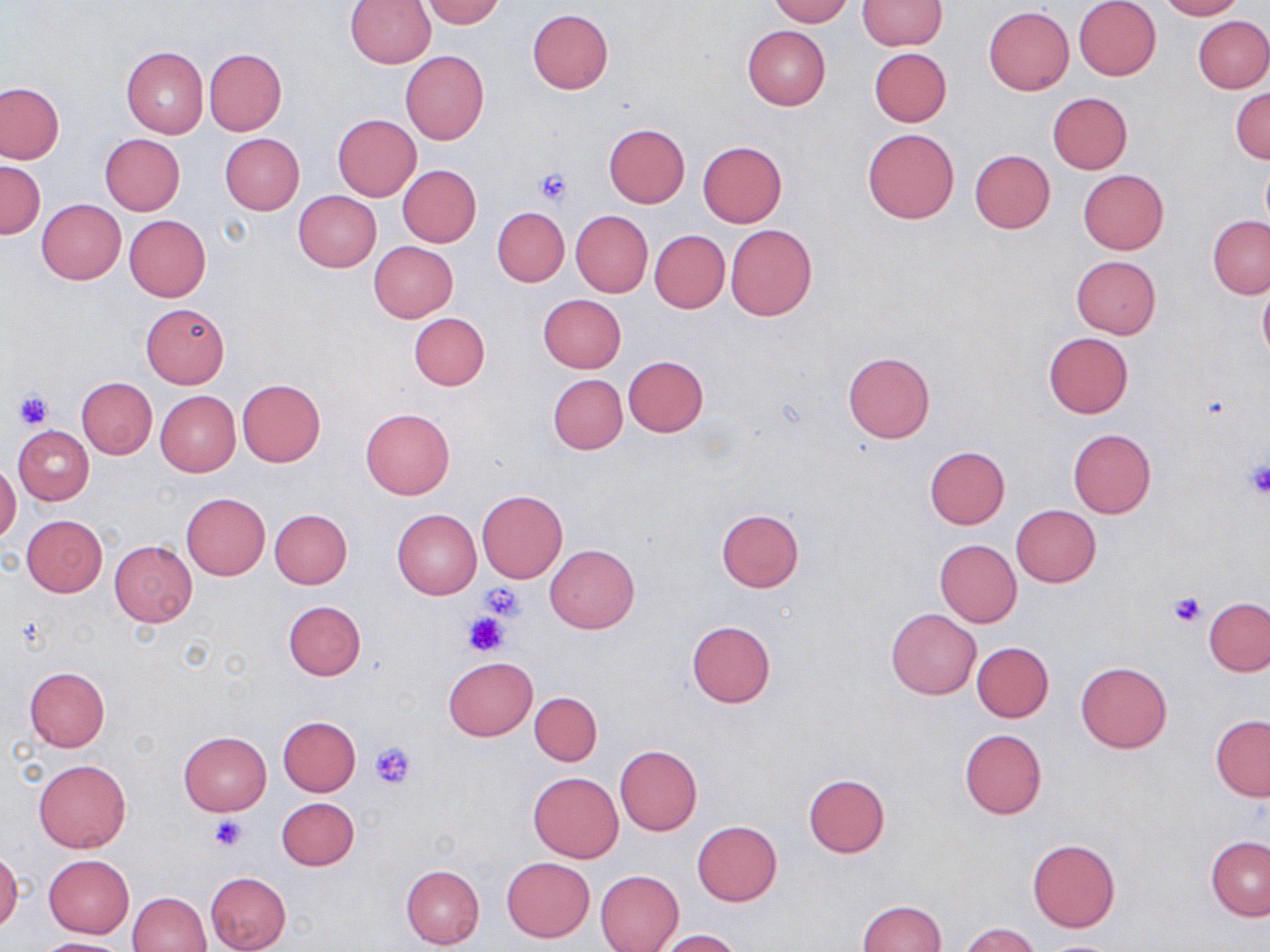 Approximate bounding boxes as named x1/y1/x2/y2 corners in pixels. Uninfected red blood cell locations: (x1=421, y1=0, x2=505, y2=28), (x1=769, y1=0, x2=853, y2=25), (x1=1073, y1=0, x2=1161, y2=80), (x1=1156, y1=0, x2=1244, y2=20), (x1=345, y1=1, x2=436, y2=66), (x1=857, y1=1, x2=946, y2=50), (x1=984, y1=6, x2=1074, y2=95), (x1=526, y1=9, x2=614, y2=94), (x1=1193, y1=15, x2=1270, y2=93), (x1=742, y1=26, x2=831, y2=109), (x1=121, y1=46, x2=208, y2=138), (x1=867, y1=47, x2=951, y2=127), (x1=203, y1=48, x2=287, y2=135), (x1=401, y1=51, x2=489, y2=146), (x1=1, y1=82, x2=65, y2=164), (x1=1231, y1=88, x2=1270, y2=163), (x1=1048, y1=91, x2=1132, y2=173), (x1=332, y1=114, x2=422, y2=200), (x1=603, y1=123, x2=690, y2=207), (x1=862, y1=128, x2=958, y2=224), (x1=100, y1=133, x2=186, y2=215), (x1=219, y1=133, x2=304, y2=215), (x1=697, y1=141, x2=787, y2=228), (x1=970, y1=149, x2=1055, y2=234), (x1=1260, y1=158, x2=1270, y2=235), (x1=0, y1=160, x2=44, y2=238), (x1=398, y1=165, x2=481, y2=247), (x1=1078, y1=169, x2=1168, y2=255), (x1=293, y1=190, x2=381, y2=272), (x1=36, y1=199, x2=125, y2=284), (x1=491, y1=207, x2=569, y2=287), (x1=571, y1=210, x2=653, y2=298), (x1=124, y1=215, x2=211, y2=301), (x1=1208, y1=216, x2=1270, y2=299), (x1=724, y1=224, x2=817, y2=320), (x1=650, y1=230, x2=730, y2=313), (x1=369, y1=241, x2=458, y2=322), (x1=1071, y1=255, x2=1161, y2=339), (x1=1258, y1=281, x2=1270, y2=365), (x1=538, y1=294, x2=626, y2=373), (x1=140, y1=302, x2=231, y2=388), (x1=409, y1=313, x2=489, y2=391), (x1=1043, y1=332, x2=1133, y2=418), (x1=843, y1=351, x2=935, y2=442), (x1=623, y1=355, x2=708, y2=436), (x1=548, y1=374, x2=627, y2=453), (x1=76, y1=377, x2=157, y2=458), (x1=236, y1=379, x2=326, y2=468), (x1=155, y1=390, x2=240, y2=476), (x1=360, y1=408, x2=455, y2=499), (x1=13, y1=426, x2=93, y2=505), (x1=1068, y1=429, x2=1157, y2=518), (x1=924, y1=446, x2=1009, y2=529), (x1=0, y1=463, x2=21, y2=545), (x1=476, y1=491, x2=567, y2=582), (x1=180, y1=493, x2=270, y2=579), (x1=1010, y1=504, x2=1101, y2=587), (x1=715, y1=508, x2=805, y2=593), (x1=270, y1=509, x2=352, y2=589), (x1=392, y1=509, x2=481, y2=600), (x1=22, y1=515, x2=107, y2=596), (x1=934, y1=539, x2=1021, y2=627), (x1=110, y1=540, x2=198, y2=626), (x1=545, y1=544, x2=638, y2=633), (x1=1204, y1=597, x2=1270, y2=677), (x1=283, y1=600, x2=365, y2=679), (x1=885, y1=608, x2=981, y2=700), (x1=687, y1=620, x2=776, y2=707), (x1=972, y1=642, x2=1053, y2=722), (x1=443, y1=656, x2=537, y2=740), (x1=1076, y1=661, x2=1172, y2=754), (x1=25, y1=667, x2=109, y2=751), (x1=530, y1=692, x2=602, y2=765), (x1=1210, y1=715, x2=1270, y2=800), (x1=278, y1=716, x2=361, y2=796), (x1=959, y1=729, x2=1047, y2=819), (x1=179, y1=731, x2=271, y2=815), (x1=614, y1=745, x2=702, y2=835), (x1=34, y1=758, x2=131, y2=853), (x1=527, y1=772, x2=623, y2=863), (x1=802, y1=773, x2=890, y2=858), (x1=276, y1=798, x2=359, y2=871), (x1=692, y1=820, x2=782, y2=906), (x1=1206, y1=836, x2=1270, y2=920), (x1=1027, y1=838, x2=1121, y2=931), (x1=0, y1=849, x2=22, y2=933), (x1=44, y1=855, x2=134, y2=937), (x1=502, y1=857, x2=595, y2=942), (x1=400, y1=865, x2=485, y2=950), (x1=596, y1=870, x2=684, y2=952), (x1=205, y1=871, x2=290, y2=951), (x1=128, y1=891, x2=211, y2=952), (x1=856, y1=899, x2=945, y2=952), (x1=960, y1=923, x2=1039, y2=952), (x1=655, y1=929, x2=743, y2=952), (x1=32, y1=937, x2=132, y2=952), (x1=1036, y1=940, x2=1125, y2=952). Platelet locations: (x1=533, y1=167, x2=572, y2=206), (x1=14, y1=390, x2=52, y2=429), (x1=1243, y1=461, x2=1270, y2=498), (x1=477, y1=585, x2=526, y2=623), (x1=1166, y1=591, x2=1208, y2=628), (x1=462, y1=610, x2=508, y2=655), (x1=370, y1=742, x2=415, y2=791), (x1=208, y1=816, x2=249, y2=852). Slide-level diagnosis: no evidence of blood parasites. Captured at 1000x magnification. Single field of view. Image is 1270×952 pixels. Thin blood smear. May-Grünwald-Giemsa stain. Optical microscopy.